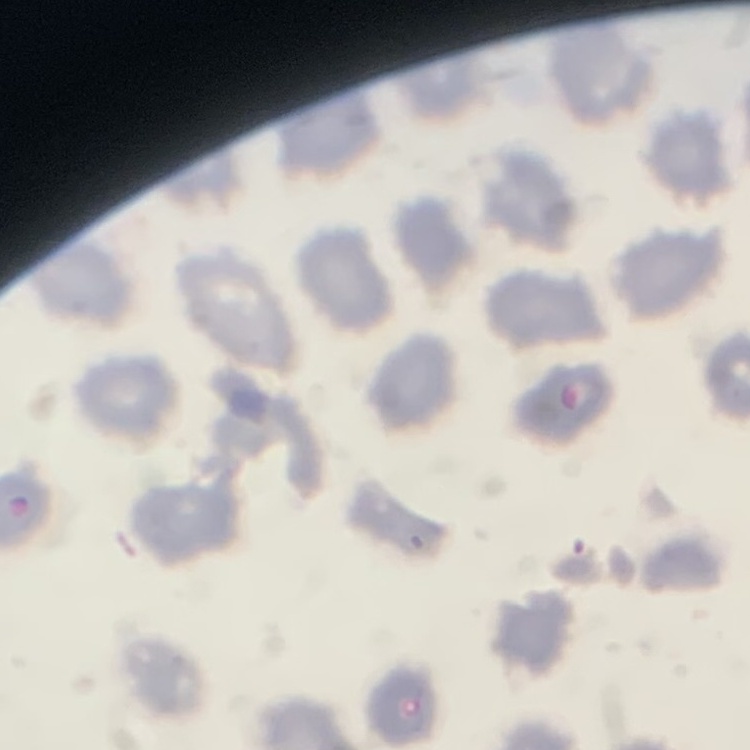

Summary:
  - Erythrocyte morphology: no rouleaux formation
  - Stain: Field's or Giemsa
  - Image type: square crop of a larger photomicrograph
  - Preparation: thin peripheral smear